Comment on the morphology of the red blood cells.
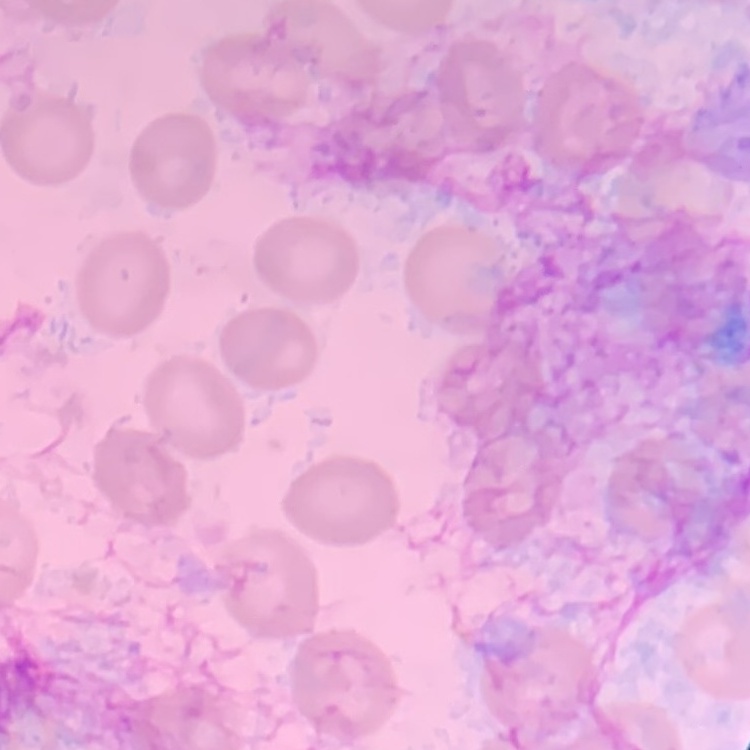

They show no rouleaux formation.

preparation: thin peripheral smear
stain: Field's or Giemsa
image_type: square crop of a larger photomicrograph